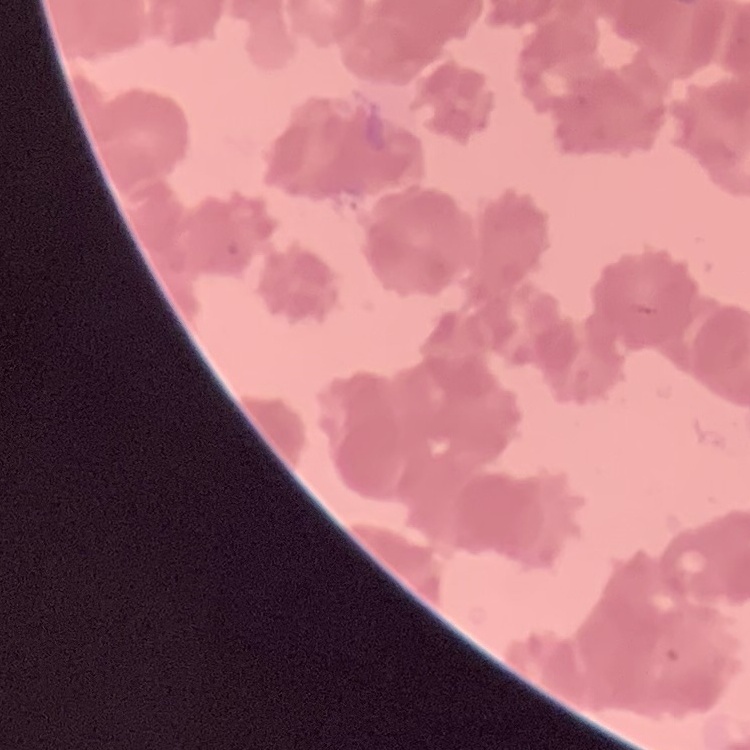

red blood cell morphology = rouleaux formation
preparation = thin blood smear
stain = Field's or Giemsa
image type = square crop of a larger photomicrograph